Identify the blood parasite species.
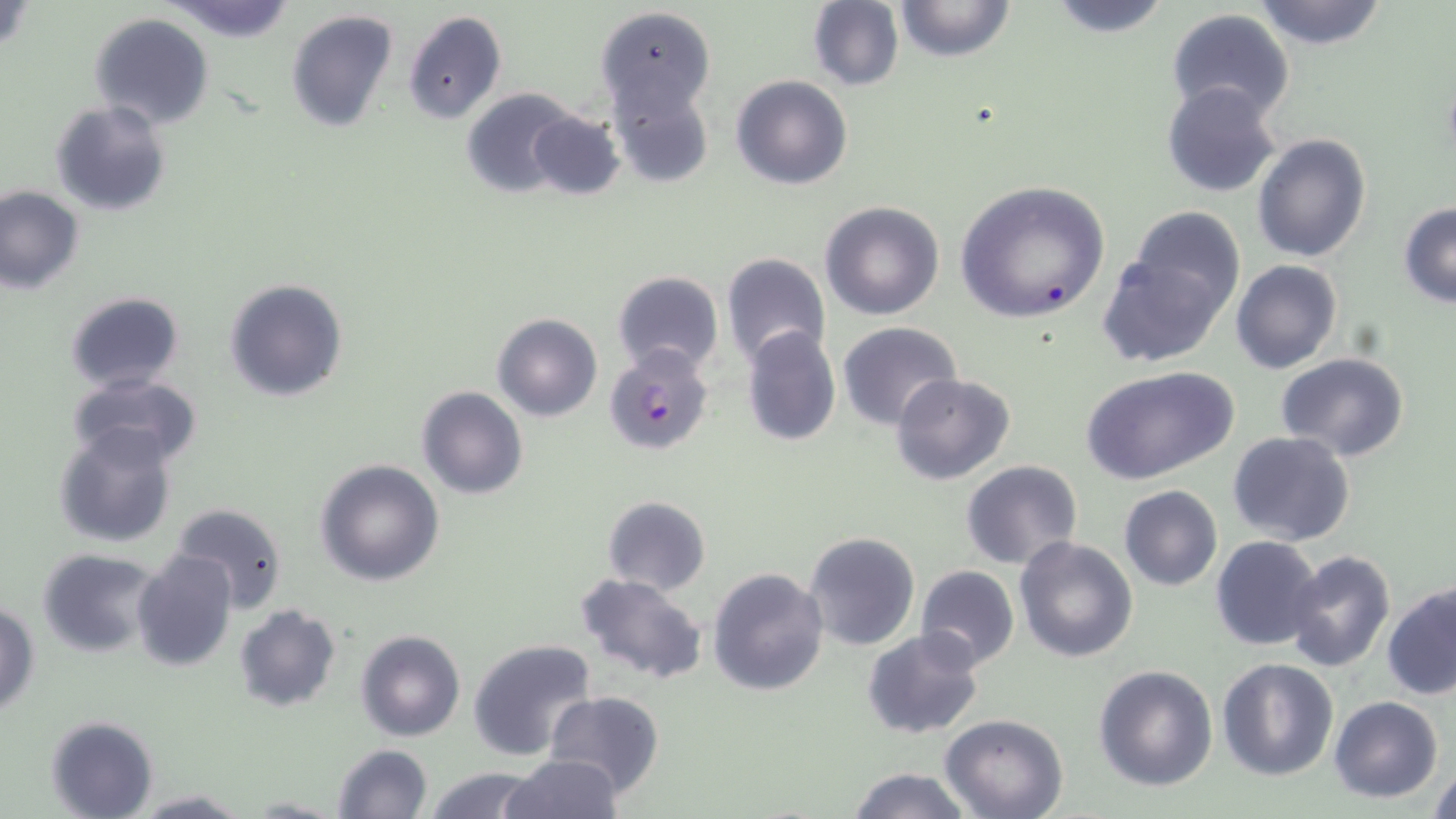

Plasmodium falciparum.

Summary:
  - Coordinate format: approximate bounding boxes as (x1, y1, x2, y2) in pixels
  - Plasmodium falciparum-infected red blood cell locations: (604, 345, 713, 456)
  - Uninfected red blood cell locations: (891, 0, 1017, 63), (1043, 0, 1174, 37), (1252, 0, 1390, 50), (165, 1, 298, 44), (806, 1, 904, 90), (594, 6, 717, 119), (1166, 9, 1296, 124), (285, 10, 398, 135), (403, 10, 507, 124), (89, 11, 215, 129), (731, 74, 853, 190), (607, 78, 715, 189), (1161, 82, 1283, 198), (461, 88, 583, 196), (50, 101, 173, 217), (528, 110, 625, 201), (1252, 132, 1372, 262), (955, 180, 1110, 326), (1, 185, 83, 294), (819, 200, 945, 320), (1398, 203, 1455, 308), (1124, 206, 1247, 325), (1100, 240, 1231, 368), (720, 252, 830, 372), (1231, 259, 1341, 373), (611, 270, 724, 376), (224, 279, 349, 403), (64, 291, 183, 393), (493, 314, 602, 422), (837, 322, 962, 430), (740, 326, 842, 448), (1274, 353, 1409, 460), (1080, 364, 1240, 486), (68, 372, 202, 469), (890, 373, 1016, 485), (415, 386, 528, 499), (52, 424, 181, 549), (1228, 432, 1356, 545), (314, 458, 445, 586), (960, 460, 1084, 570), (1118, 485, 1222, 590), (602, 495, 711, 595), (1134, 499, 1272, 615), (169, 502, 290, 614), (803, 531, 921, 651), (1014, 535, 1140, 662), (1211, 536, 1325, 653), (36, 548, 164, 659), (132, 549, 237, 671), (1284, 551, 1397, 674), (915, 564, 1018, 670), (707, 566, 830, 697), (573, 571, 709, 684), (1383, 580, 1456, 701), (1, 601, 39, 717), (233, 604, 341, 713), (861, 629, 986, 741), (355, 630, 466, 742), (467, 638, 597, 762), (1217, 657, 1339, 781), (1093, 664, 1218, 791), (544, 690, 664, 800), (1329, 696, 1443, 803), (940, 714, 1068, 819), (45, 715, 158, 819), (330, 743, 433, 819), (501, 754, 623, 819), (423, 766, 543, 819), (848, 767, 971, 819), (1426, 767, 1456, 817), (129, 790, 253, 817), (243, 794, 345, 817)
  - Field of view: single
  - Modality: light microscopy
  - Stain: May-Grünwald-Giemsa
  - Image size: 1456×819 pixels
  - Preparation: thin blood smear
  - Magnification: 1000x